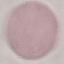
Malaria status: uninfected. Cell patch, automatically extracted from a larger field of view and resized to 64 × 64 pixels. Thin blood smear. Giemsa-stained preparation. Acquired by smartphone through the microscope eyepiece.